Classify this cell by malaria status.
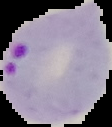
It is parasitized.

Summary:
  - Image type: cell region segmented out of the field of view; surrounding area masked to black
  - Image size: 112×127 pixels
  - Preparation: thin blood smear